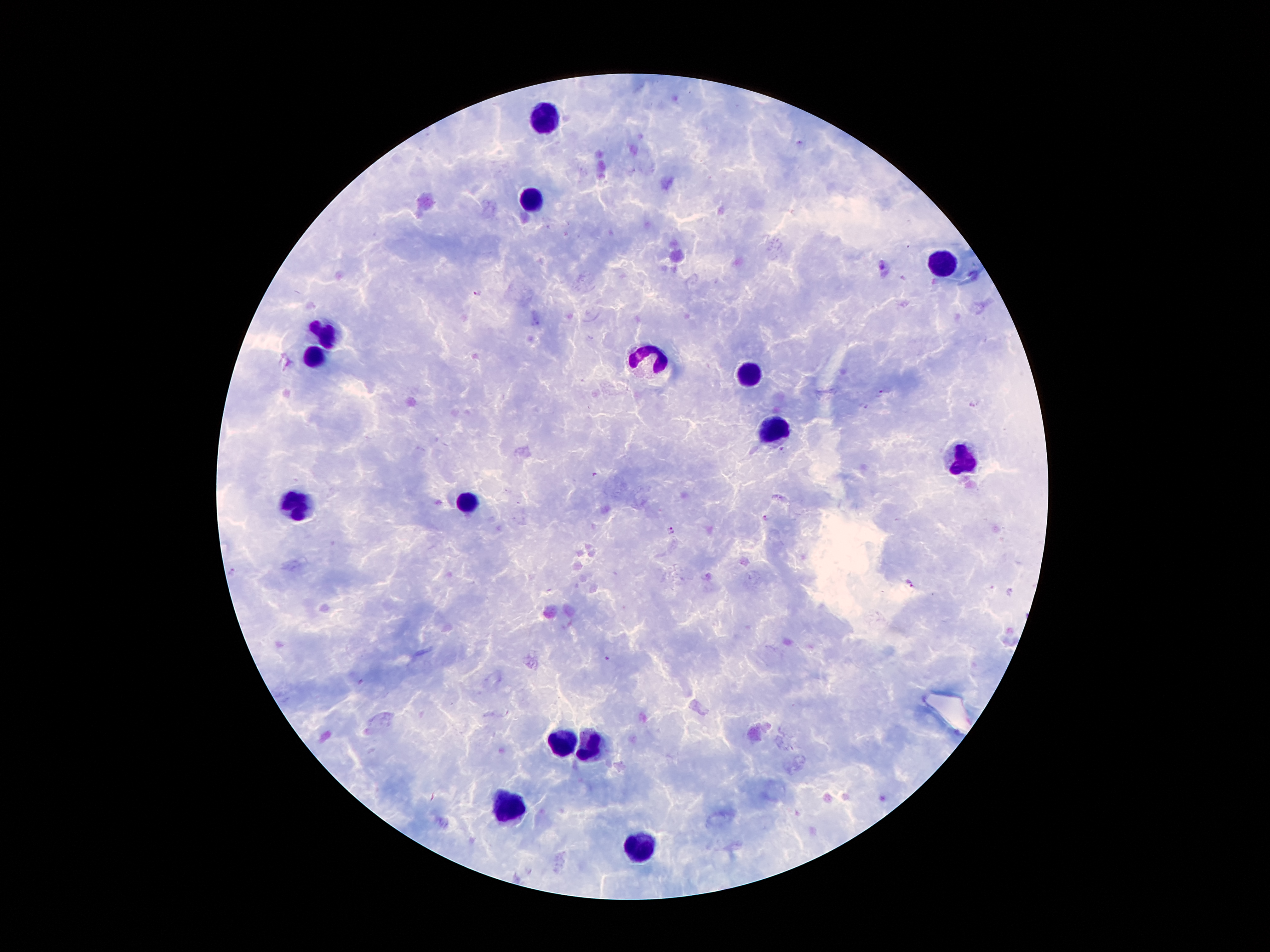
Approximate centers as {x, y} in pixels.
Summary:
  - Leukocyte locations: {541, 116}, {529, 200}, {942, 261}, {327, 337}, {314, 355}, {655, 366}, {749, 374}, {772, 431}, {963, 460}, {468, 502}, {293, 509}, {558, 746}, {594, 750}, {508, 811}, {640, 849}
  - Malaria parasite locations: {477, 293}, {880, 394}, {974, 402}, {863, 406}, {782, 450}, {594, 475}, {766, 518}, {671, 531}, {909, 583}, {606, 658}
  - Field of view: single
  - Magnification: 100x
  - Patient malaria status: infected with Plasmodium falciparum
  - Capture: smartphone through the microscope eyepiece
  - Image size: 1270×952 pixels
  - Stain: Giemsa
  - Preparation: thick blood film